Give the position of every Plasmodium parasite.
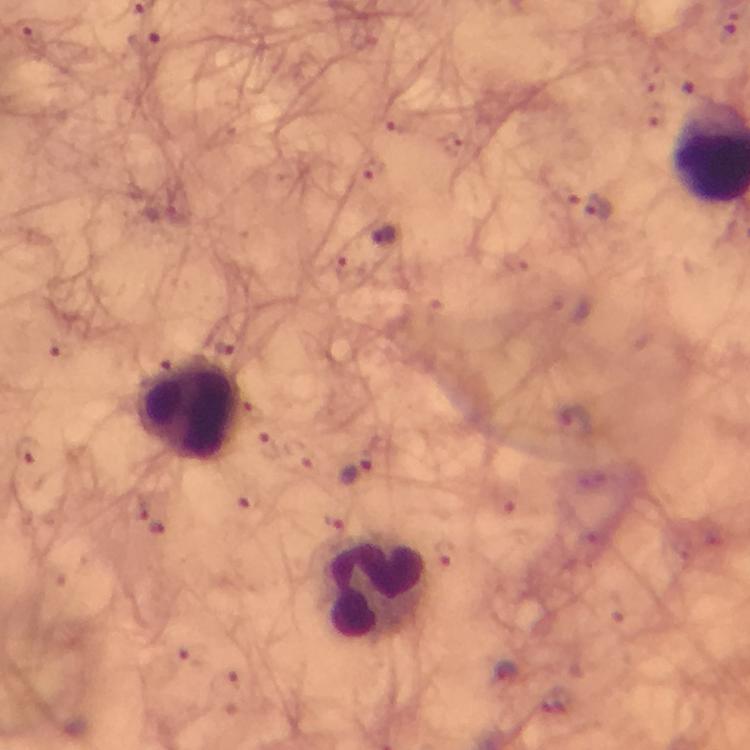

Approximate centers as (x, y) in pixels.
Plasmodium parasites: (146, 42), (601, 210), (383, 237), (356, 472).

Summary:
  - Leukocyte locations: (191, 410), (373, 587)
  - Immersion oil: used
  - Magnification: 100x
  - Context: from a malaria diagnostic workup
  - Stain: Giemsa
  - Cropped from: one field of view
  - Image size: 750×750 pixels
  - Preparation: thick blood film
  - Capture: smartphone mounted on the microscope